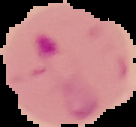

{
  "image_size": "136×127 pixels",
  "malaria_status": "parasitized",
  "image_type": "segmented cell region on a black background",
  "preparation": "thin blood smear"
}